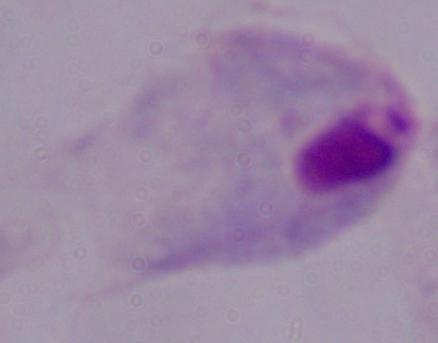
Summary:
  - Identification: trichomonad
  - Magnification: 1000x
  - Modality: micrograph